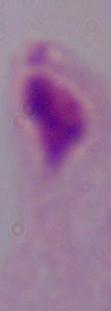
Summary:
  - Modality: micrograph
  - Identification: trichomonad
  - Magnification: 1000x